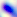

Summary:
  - Magnification: 400x
  - Modality: photomicrograph
  - Identification: Toxoplasma gondii